Report the malaria status of this cell.
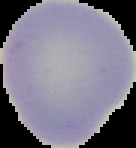

Uninfected.

image size = 136×148 pixels
preparation = thin blood film
image type = segmented cell region on a black background